State which cell type is depicted.
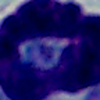
A leukocyte.

{
  "magnification": "1000x",
  "modality": "micrograph"
}